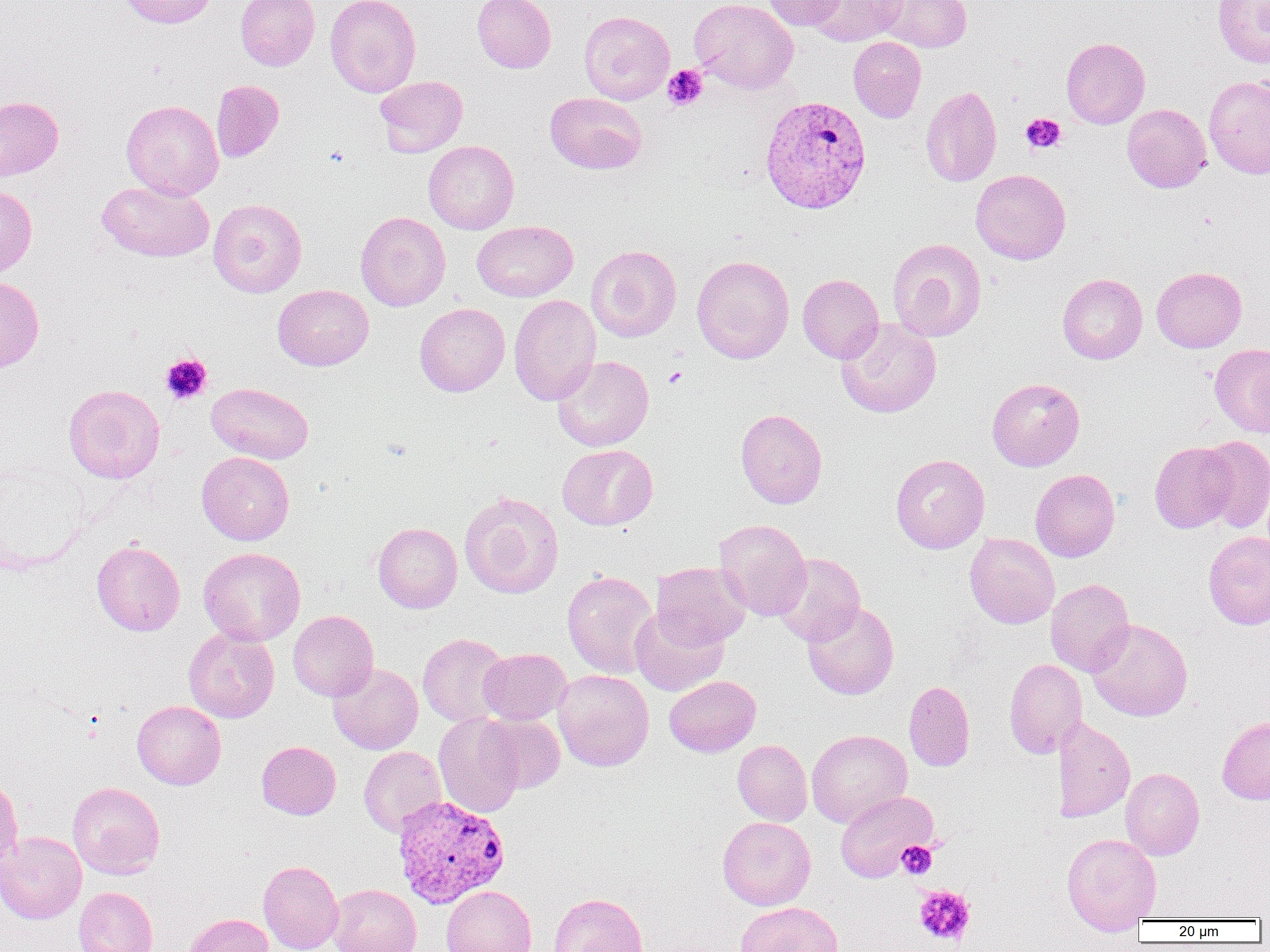

Summary:
  - Coordinate format: approximate bounding boxes as (x1,y1)-(x2,y2) corner pairs in pixels
  - Platelet locations: (662,64)-(709,111), (1021,113)-(1066,153), (160,353)-(212,404), (662,365)-(687,389), (897,841)-(937,879), (913,885)-(976,947)
  - Uninfected red blood cell locations: (117,0)-(218,28), (235,0)-(320,71), (325,0)-(421,97), (472,0)-(555,73), (690,0)-(798,94), (763,0)-(846,30), (805,0)-(908,46), (876,0)-(972,53), (1213,0)-(1270,68), (579,11)-(674,104), (848,37)-(926,122), (1061,37)-(1150,129), (1203,74)-(1270,178), (374,75)-(468,157), (211,79)-(284,163), (921,85)-(1002,187), (545,93)-(647,174), (0,96)-(63,181), (121,99)-(224,201), (1122,103)-(1211,193), (424,140)-(519,234), (971,169)-(1071,265), (97,180)-(214,263), (0,185)-(37,278), (208,198)-(307,297), (355,211)-(451,311), (472,220)-(577,302), (886,238)-(986,341), (586,245)-(682,342), (692,255)-(794,364), (1152,266)-(1247,353), (797,273)-(884,363), (1057,273)-(1147,364), (0,276)-(44,373), (273,284)-(374,371), (509,294)-(601,405), (414,302)-(510,397), (835,318)-(942,418), (1209,343)-(1270,437), (552,355)-(653,451), (987,378)-(1085,471), (206,382)-(314,463), (63,384)-(165,483), (735,409)-(827,508), (1197,436)-(1270,533), (1149,441)-(1238,533), (557,444)-(657,530), (197,452)-(294,545), (890,454)-(990,554), (1030,469)-(1120,562), (459,491)-(563,598), (714,519)-(812,620), (373,522)-(462,613), (1203,531)-(1270,630), (964,533)-(1060,628), (91,540)-(185,636), (199,547)-(305,646), (773,553)-(865,645), (650,561)-(751,649), (562,570)-(657,678), (1045,579)-(1134,677), (802,601)-(899,700), (630,607)-(728,696), (288,611)-(378,701), (1087,619)-(1193,721), (183,628)-(279,723), (417,633)-(511,727), (478,648)-(571,725), (1004,658)-(1088,758), (328,663)-(423,754), (552,669)-(654,771), (664,675)-(761,757), (904,680)-(975,771), (132,700)-(225,789), (478,712)-(566,793), (433,713)-(525,819), (1217,715)-(1270,805), (1052,717)-(1135,822), (806,729)-(912,827), (732,739)-(812,826), (256,741)-(341,820), (359,746)-(446,837), (1120,767)-(1204,860), (0,775)-(23,873), (67,782)-(165,879), (835,790)-(938,882), (717,816)-(816,910), (0,831)-(86,924), (1061,832)-(1162,932), (258,860)-(343,952), (328,884)-(421,952), (441,885)-(537,952), (74,886)-(158,952), (548,892)-(648,952), (736,901)-(843,952), (181,913)-(274,952)
  - Plasmodium vivax-infected red blood cell locations: (759,95)-(872,214), (391,794)-(510,909)
  - Slide-level diagnosis: Plasmodium vivax
  - Preparation: thin blood smear
  - Modality: optical microscopy
  - Field of view: single
  - Magnification: 1000x
  - Image size: 1270×952 pixels